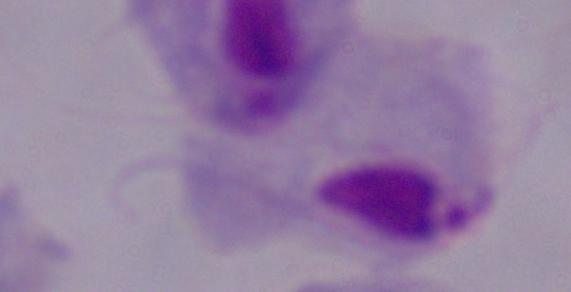

Summary:
  - Modality: photomicrograph
  - Identification: trichomonad
  - Magnification: 1000x